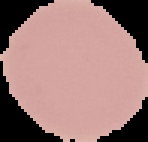
Summary:
  - Preparation: thin blood film
  - Image type: segmented cell region on a black background
  - Malaria status: uninfected
  - Image size: 148×142 pixels